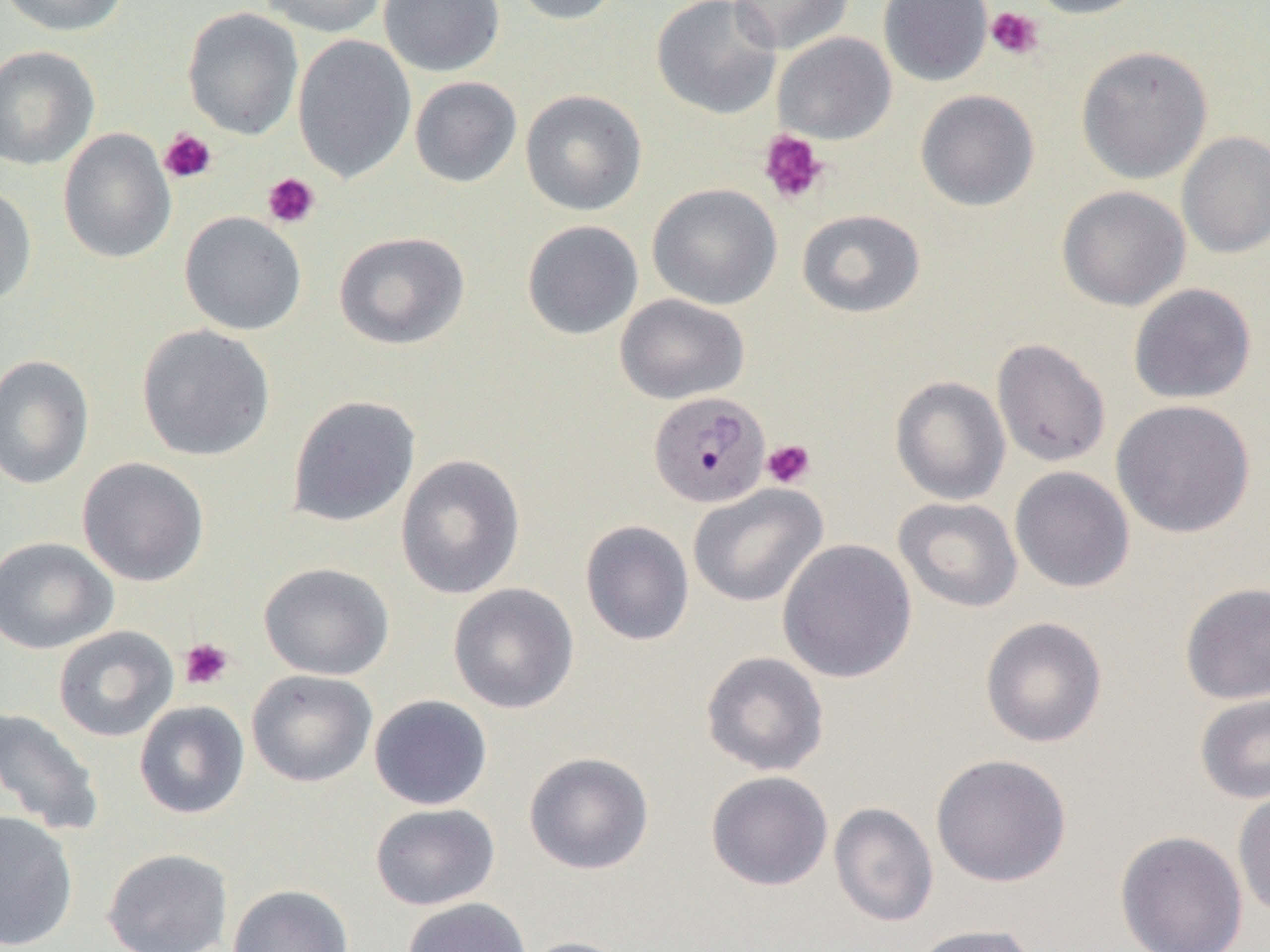

Approximate bounding boxes as (x1, y1, x2, y2) in pixels. Uninfected red blood cell locations: (1, 0, 130, 37), (257, 0, 389, 37), (378, 0, 505, 77), (507, 0, 623, 26), (651, 0, 782, 120), (728, 0, 854, 55), (879, 0, 993, 86), (1022, 0, 1153, 19), (182, 8, 303, 140), (773, 32, 897, 144), (292, 35, 416, 184), (0, 45, 100, 171), (1076, 45, 1213, 184), (409, 76, 522, 188), (520, 89, 648, 216), (915, 89, 1040, 211), (58, 128, 176, 264), (1177, 131, 1270, 259), (647, 183, 782, 310), (0, 185, 37, 307), (1057, 186, 1190, 311), (796, 209, 925, 318), (178, 211, 307, 335), (522, 220, 644, 340), (333, 231, 470, 350), (1128, 283, 1257, 405), (614, 294, 750, 405), (136, 324, 276, 461), (990, 338, 1111, 468), (0, 355, 94, 490), (890, 375, 1011, 505), (286, 395, 421, 527), (1111, 399, 1256, 539), (395, 454, 525, 600), (77, 456, 210, 586), (1009, 466, 1135, 593), (688, 484, 827, 608), (893, 496, 1023, 613), (579, 520, 695, 647), (0, 536, 118, 655), (777, 539, 918, 684), (258, 561, 395, 680), (1179, 581, 1270, 705), (447, 583, 579, 714), (979, 616, 1108, 748), (53, 626, 178, 742), (700, 651, 830, 776), (246, 669, 377, 787), (1194, 692, 1270, 805), (368, 694, 493, 810), (134, 700, 251, 820), (0, 707, 104, 837), (523, 751, 655, 875), (930, 753, 1072, 887), (705, 770, 833, 891), (1232, 787, 1270, 921), (829, 802, 939, 927), (370, 803, 500, 910), (0, 810, 79, 950), (1115, 830, 1248, 952), (102, 847, 234, 952), (227, 884, 353, 952), (401, 897, 532, 952), (907, 923, 1041, 952), (517, 936, 636, 952). Plasmodium malariae-infected red blood cell locations: (648, 390, 770, 508). Platelet locations: (985, 6, 1044, 60), (159, 129, 217, 184), (758, 130, 829, 206), (262, 173, 321, 228), (761, 439, 816, 489), (179, 638, 234, 690). Slide-level diagnosis: Plasmodium malariae. One field of a larger specimen. Thin blood film. Image is 1270×952 pixels. Captured at 1000x magnification. Optical microscopy.